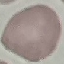

Summary:
  - Malaria status: uninfected
  - Capture: smartphone camera at the microscope eyepiece
  - Preparation: thin blood film
  - Image type: automatically extracted cell patch, resized to 64 × 64 pixels
  - Stain: Giemsa